Describe the morphology of the red blood cells.
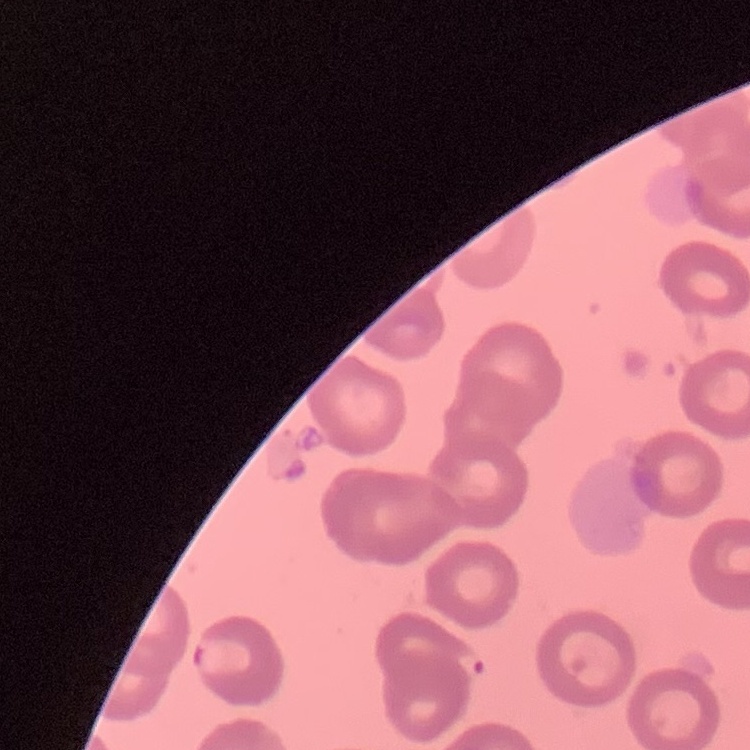
They show no rouleaux formation.

Summary:
  - Image type: one tile cut from a larger photomicrograph
  - Stain: Field's or Giemsa
  - Preparation: thin blood film